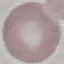
Summary:
  - Result: negative for malaria parasites
  - Stain: Giemsa
  - Preparation: thin smear
  - Capture: smartphone camera at the microscope eyepiece
  - Image type: automatically extracted cell patch, resized to 64 × 64 pixels